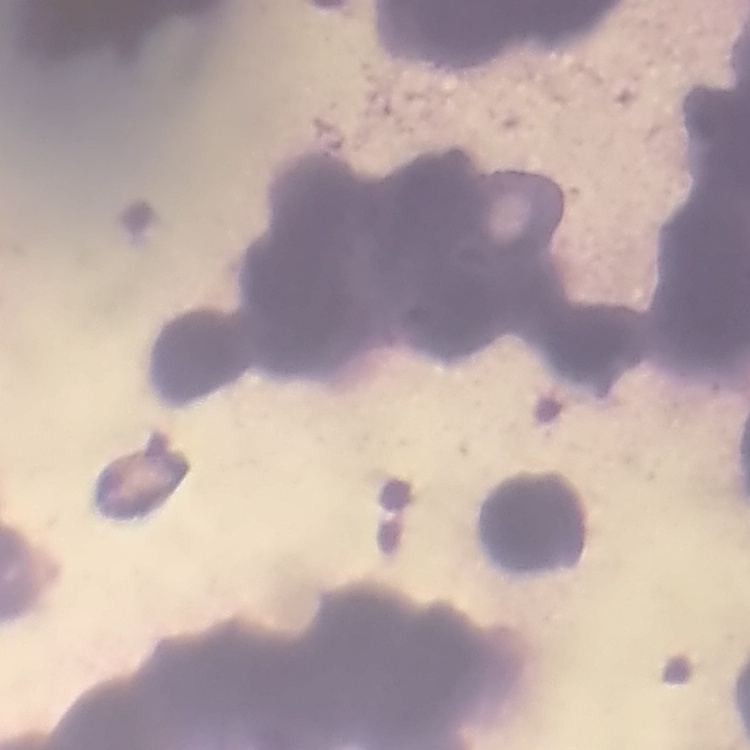

The erythrocytes exhibit rouleaux formation. Thin peripheral smear. One tile cut from a larger photomicrograph. Field's or Giemsa stain.